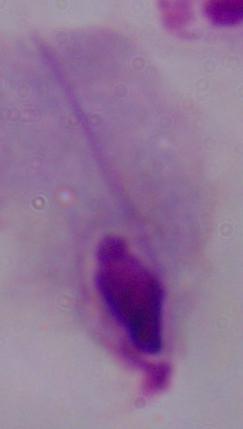 1000x magnification. Photomicrograph. A trichomonad is shown.